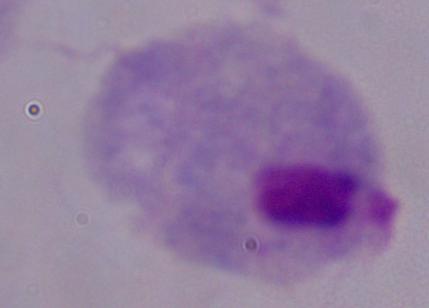 A trichomonad is shown. Photomicrograph. Captured at 1000x magnification.